Assess this cell for malaria.
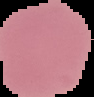
Uninfected.

Cell region segmented out of the field of view; the surrounding area is masked to black. From a thin blood smear. Image is 94×97 pixels.